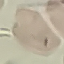

Malaria status: uninfected. Giemsa stain. Acquired by smartphone through the microscope eyepiece. Cell patch, automatically extracted from a larger field of view and resized to 64 × 64 pixels. Thin blood film.